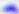
magnification = 400x
identification = Toxoplasma gondii
modality = photomicrograph